Report the malaria status of this cell.
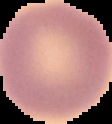
It is uninfected.

The area outside the segmented cell region is set to black. From a thin blood smear. Image is 112×124 pixels.